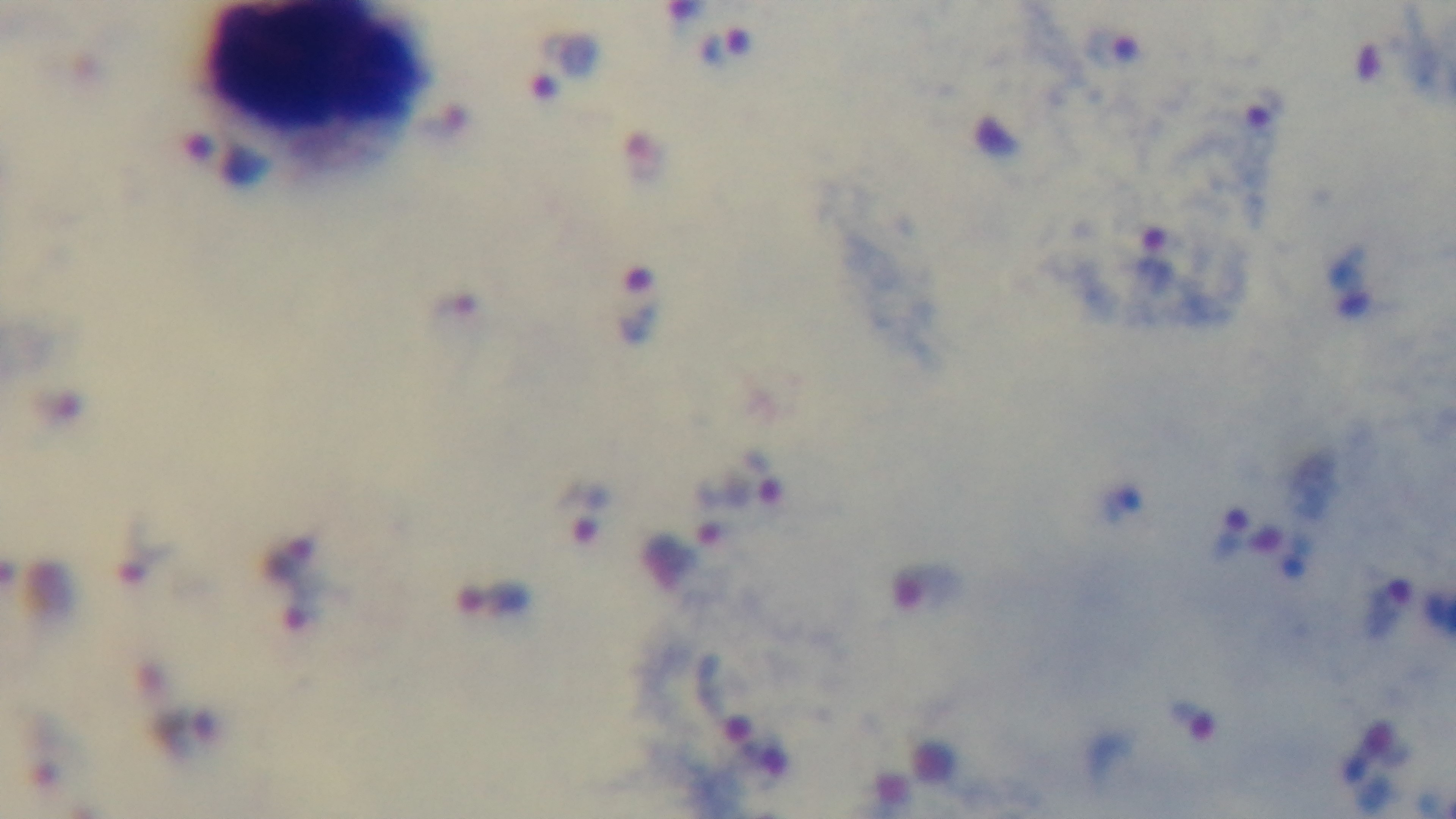

Summary:
  - Objective: 100x oil immersion
  - Preparation: thick
  - Modality: light microscopy
  - Stain: Giemsa
  - Capture: mounted 4K digital camera
  - Field of view: one from the slide
  - Malaria status: positive